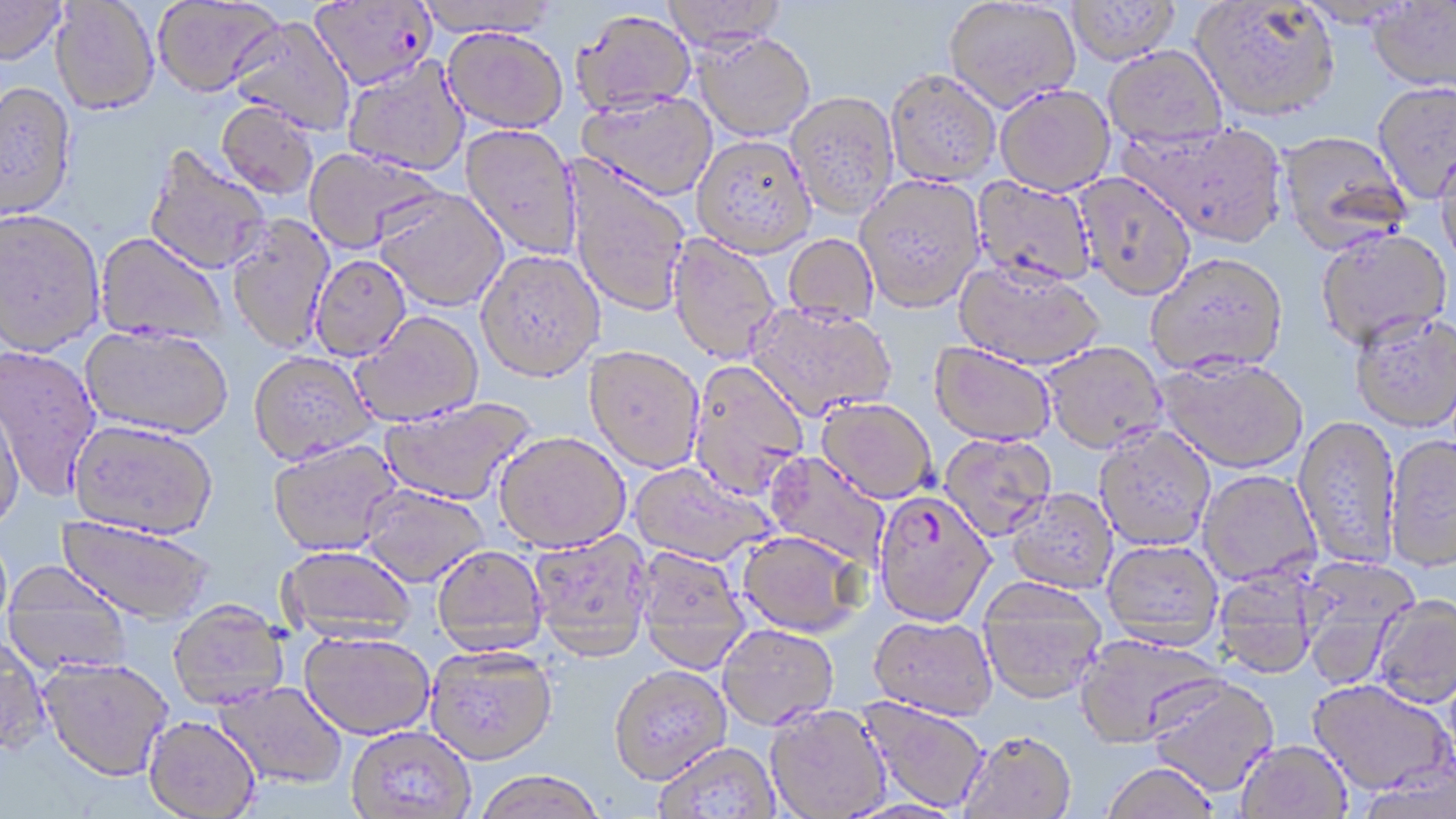
Summary:
  - Coordinate format: approximate bounding boxes as named x1/y1/x2/y2 corners in pixels
  - Plasmodium falciparum-infected red blood cell locations: (x1=309, y1=0, x2=438, y2=90), (x1=872, y1=491, x2=995, y2=626)
  - Uninfected red blood cell locations: (x1=0, y1=0, x2=66, y2=66), (x1=50, y1=0, x2=160, y2=116), (x1=153, y1=0, x2=283, y2=97), (x1=413, y1=0, x2=561, y2=36), (x1=661, y1=0, x2=788, y2=51), (x1=944, y1=0, x2=1081, y2=111), (x1=1067, y1=1, x2=1180, y2=64), (x1=1192, y1=1, x2=1341, y2=121), (x1=1367, y1=1, x2=1456, y2=92), (x1=570, y1=9, x2=697, y2=115), (x1=227, y1=16, x2=356, y2=137), (x1=442, y1=26, x2=569, y2=133), (x1=693, y1=32, x2=817, y2=141), (x1=1103, y1=46, x2=1228, y2=149), (x1=342, y1=55, x2=471, y2=176), (x1=885, y1=69, x2=1001, y2=186), (x1=1372, y1=80, x2=1456, y2=203), (x1=0, y1=82, x2=77, y2=222), (x1=994, y1=84, x2=1115, y2=196), (x1=577, y1=90, x2=718, y2=201), (x1=786, y1=90, x2=899, y2=220), (x1=216, y1=100, x2=319, y2=200), (x1=1123, y1=120, x2=1289, y2=247), (x1=460, y1=124, x2=582, y2=261), (x1=1276, y1=130, x2=1412, y2=254), (x1=692, y1=135, x2=817, y2=258), (x1=1434, y1=144, x2=1456, y2=267), (x1=143, y1=145, x2=272, y2=275), (x1=303, y1=148, x2=445, y2=255), (x1=566, y1=160, x2=691, y2=318), (x1=1074, y1=172, x2=1196, y2=300), (x1=854, y1=173, x2=985, y2=312), (x1=970, y1=175, x2=1097, y2=288), (x1=374, y1=189, x2=508, y2=312), (x1=0, y1=210, x2=105, y2=356), (x1=226, y1=215, x2=335, y2=354), (x1=1315, y1=227, x2=1452, y2=349), (x1=94, y1=233, x2=227, y2=345), (x1=783, y1=233, x2=879, y2=326), (x1=667, y1=235, x2=781, y2=364), (x1=476, y1=251, x2=605, y2=383), (x1=1146, y1=251, x2=1288, y2=374), (x1=309, y1=255, x2=411, y2=362), (x1=954, y1=260, x2=1106, y2=370), (x1=746, y1=302, x2=896, y2=420), (x1=1350, y1=310, x2=1456, y2=431), (x1=350, y1=312, x2=484, y2=426), (x1=80, y1=327, x2=233, y2=441), (x1=930, y1=342, x2=1056, y2=446), (x1=1042, y1=342, x2=1167, y2=453), (x1=0, y1=345, x2=103, y2=502), (x1=583, y1=346, x2=705, y2=474), (x1=248, y1=353, x2=378, y2=467), (x1=1156, y1=356, x2=1308, y2=473), (x1=688, y1=361, x2=809, y2=499), (x1=0, y1=392, x2=25, y2=530), (x1=378, y1=397, x2=537, y2=507), (x1=815, y1=398, x2=937, y2=504), (x1=1293, y1=414, x2=1401, y2=567), (x1=67, y1=421, x2=217, y2=542), (x1=1094, y1=425, x2=1216, y2=550), (x1=493, y1=432, x2=630, y2=553), (x1=939, y1=433, x2=1057, y2=540), (x1=1384, y1=433, x2=1456, y2=571), (x1=268, y1=440, x2=403, y2=557), (x1=762, y1=452, x2=890, y2=569), (x1=628, y1=463, x2=775, y2=566), (x1=1198, y1=470, x2=1321, y2=585), (x1=359, y1=485, x2=489, y2=587), (x1=1005, y1=488, x2=1117, y2=594), (x1=56, y1=517, x2=214, y2=625), (x1=736, y1=530, x2=866, y2=638), (x1=528, y1=531, x2=653, y2=662), (x1=1102, y1=540, x2=1223, y2=647), (x1=432, y1=546, x2=547, y2=655), (x1=278, y1=547, x2=417, y2=641), (x1=634, y1=549, x2=751, y2=674), (x1=1296, y1=557, x2=1420, y2=686), (x1=1213, y1=566, x2=1318, y2=678), (x1=2, y1=570, x2=133, y2=674), (x1=977, y1=577, x2=1107, y2=703), (x1=1371, y1=593, x2=1456, y2=708), (x1=166, y1=603, x2=289, y2=710), (x1=868, y1=614, x2=998, y2=720), (x1=718, y1=624, x2=839, y2=730), (x1=299, y1=632, x2=435, y2=740), (x1=1075, y1=633, x2=1227, y2=748), (x1=0, y1=639, x2=52, y2=759), (x1=424, y1=647, x2=557, y2=766), (x1=38, y1=659, x2=173, y2=783), (x1=608, y1=667, x2=732, y2=787), (x1=1146, y1=675, x2=1279, y2=795), (x1=1308, y1=679, x2=1453, y2=795), (x1=213, y1=681, x2=347, y2=789), (x1=856, y1=697, x2=989, y2=814), (x1=764, y1=704, x2=891, y2=818), (x1=143, y1=717, x2=260, y2=819), (x1=346, y1=726, x2=477, y2=818), (x1=958, y1=731, x2=1077, y2=819), (x1=1236, y1=739, x2=1353, y2=819), (x1=654, y1=743, x2=781, y2=818), (x1=1356, y1=759, x2=1455, y2=819), (x1=1101, y1=762, x2=1219, y2=819), (x1=473, y1=772, x2=607, y2=819)
  - Slide-level diagnosis: Plasmodium falciparum
  - Stain: May-Grünwald-Giemsa
  - Modality: optical microscopy
  - Image size: 1456×819 pixels
  - Preparation: thin blood film
  - Field of view: one of a larger specimen
  - Magnification: 1000x